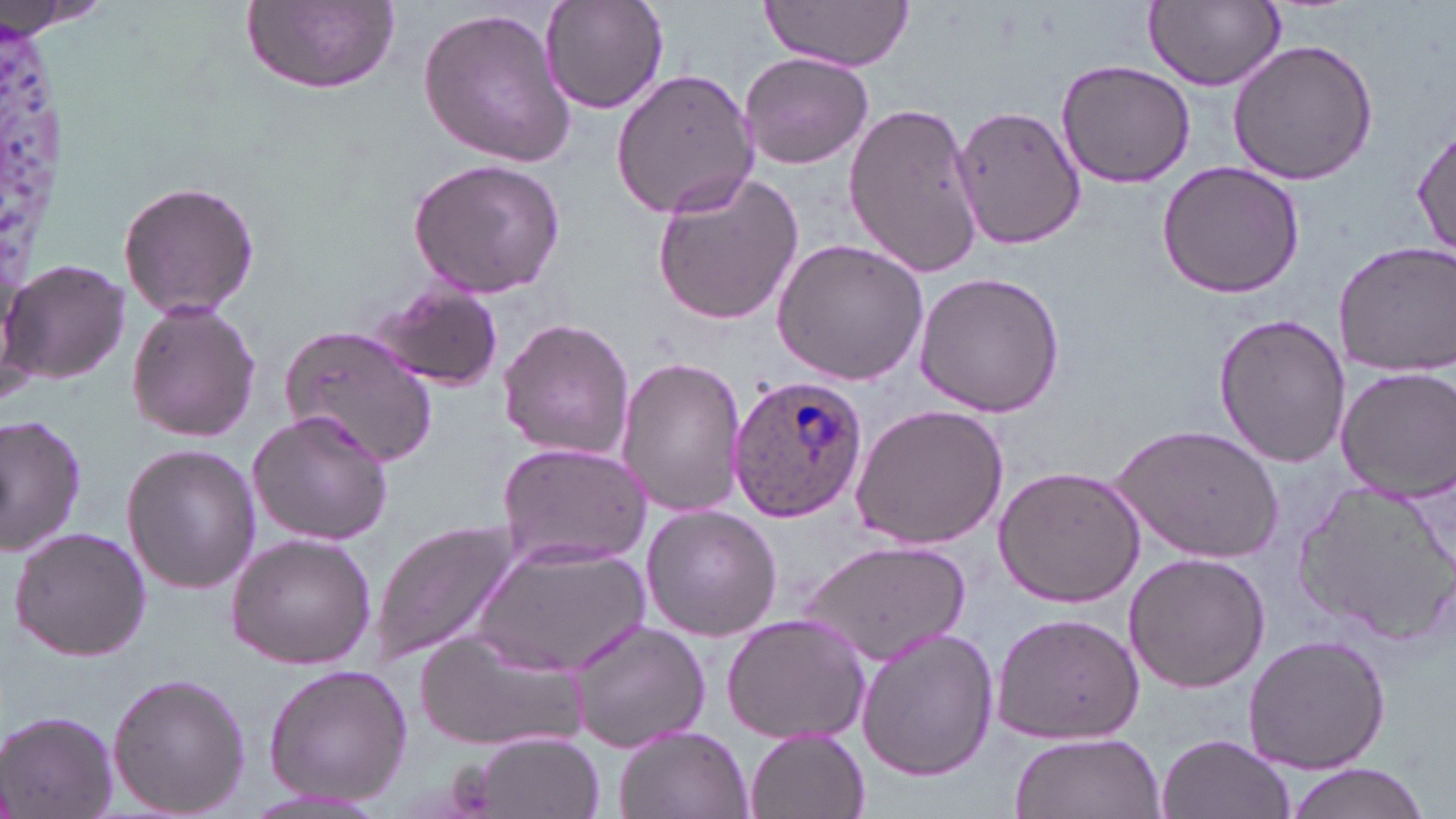
Approximate bounding boxes as named x1/y1/x2/y2 corners in pixels. White blood cell locations: (x1=0, y1=0, x2=85, y2=352). Plasmodium ovale-infected red blood cell locations: (x1=725, y1=374, x2=868, y2=524). Uninfected red blood cell locations: (x1=540, y1=0, x2=669, y2=115), (x1=0, y1=1, x2=120, y2=37), (x1=759, y1=1, x2=916, y2=70), (x1=1145, y1=1, x2=1285, y2=90), (x1=244, y1=2, x2=398, y2=95), (x1=417, y1=5, x2=577, y2=169), (x1=1226, y1=39, x2=1380, y2=187), (x1=738, y1=51, x2=873, y2=169), (x1=1054, y1=58, x2=1197, y2=190), (x1=612, y1=67, x2=761, y2=220), (x1=843, y1=101, x2=987, y2=281), (x1=952, y1=103, x2=1086, y2=252), (x1=1413, y1=122, x2=1455, y2=262), (x1=408, y1=158, x2=566, y2=296), (x1=1156, y1=161, x2=1305, y2=299), (x1=649, y1=170, x2=806, y2=328), (x1=119, y1=179, x2=259, y2=321), (x1=771, y1=237, x2=929, y2=385), (x1=1333, y1=241, x2=1456, y2=376), (x1=2, y1=258, x2=131, y2=389), (x1=913, y1=272, x2=1065, y2=418), (x1=368, y1=283, x2=504, y2=391), (x1=126, y1=300, x2=262, y2=443), (x1=1213, y1=313, x2=1351, y2=468), (x1=498, y1=316, x2=634, y2=462), (x1=281, y1=323, x2=438, y2=469), (x1=617, y1=357, x2=746, y2=516), (x1=1335, y1=365, x2=1456, y2=500), (x1=848, y1=404, x2=1009, y2=551), (x1=248, y1=407, x2=393, y2=545), (x1=1, y1=415, x2=86, y2=559), (x1=1115, y1=422, x2=1282, y2=565), (x1=497, y1=443, x2=648, y2=571), (x1=123, y1=445, x2=261, y2=594), (x1=993, y1=466, x2=1145, y2=606), (x1=1292, y1=476, x2=1455, y2=644), (x1=640, y1=505, x2=781, y2=641), (x1=369, y1=518, x2=524, y2=666), (x1=9, y1=527, x2=152, y2=661), (x1=227, y1=533, x2=376, y2=669), (x1=473, y1=539, x2=652, y2=679), (x1=801, y1=540, x2=971, y2=664), (x1=1121, y1=551, x2=1272, y2=694), (x1=988, y1=611, x2=1146, y2=746), (x1=720, y1=612, x2=873, y2=747), (x1=567, y1=617, x2=710, y2=755), (x1=855, y1=625, x2=999, y2=782), (x1=413, y1=626, x2=587, y2=752), (x1=1243, y1=632, x2=1391, y2=773), (x1=263, y1=663, x2=412, y2=803), (x1=106, y1=671, x2=250, y2=819), (x1=1, y1=709, x2=117, y2=818), (x1=612, y1=725, x2=751, y2=819), (x1=744, y1=729, x2=869, y2=819), (x1=1009, y1=732, x2=1166, y2=819), (x1=1156, y1=732, x2=1295, y2=819), (x1=473, y1=733, x2=604, y2=818), (x1=1281, y1=764, x2=1432, y2=819). Slide-level diagnosis: Plasmodium ovale. Thin blood film. May-Grünwald-Giemsa-stained preparation. 1000x magnification. One field of a larger specimen. Image is 1456×819 pixels. Optical microscopy.